Locate every Plasmodium parasite.
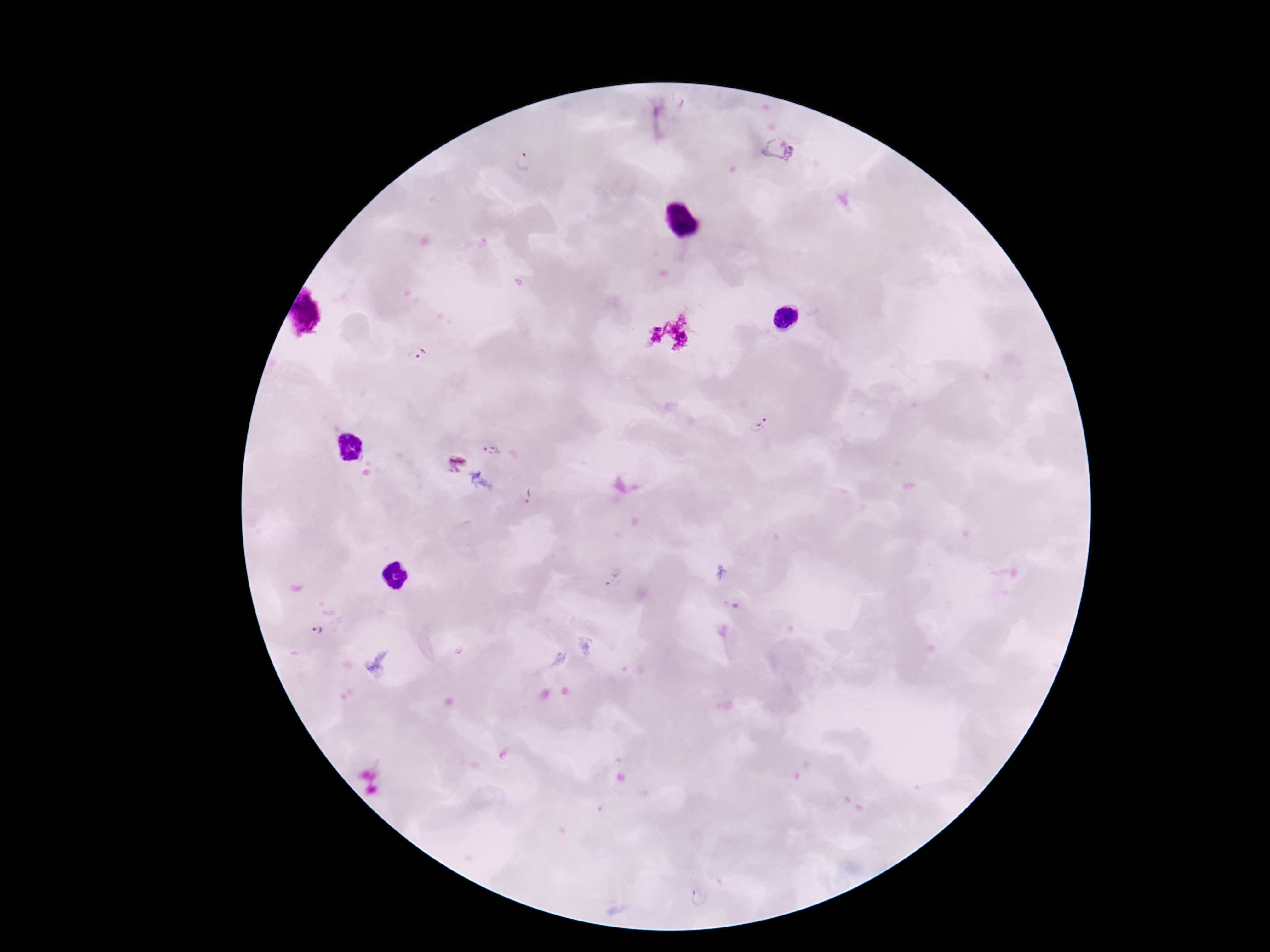

Approximate object centers, in pixels from the top-left corner.
Plasmodium parasites: (x=778, y=148), (x=525, y=162), (x=415, y=354), (x=759, y=424), (x=490, y=449), (x=454, y=463), (x=527, y=498), (x=613, y=577), (x=318, y=631), (x=700, y=898).

Thick blood film. Giemsa stain. Patient malaria status: positive. Image is 1270×952 pixels. Photographed through the microscope eyepiece with a smartphone camera. 100x magnification. Single field of view.